Name the parasite shown.
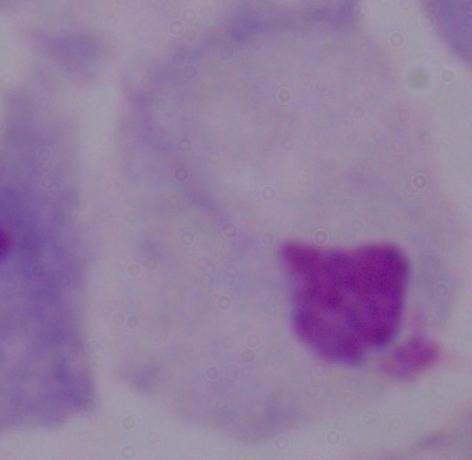

This is a trichomonad.

modality = photomicrograph
magnification = 1000x